Describe the morphology of the red blood cells.
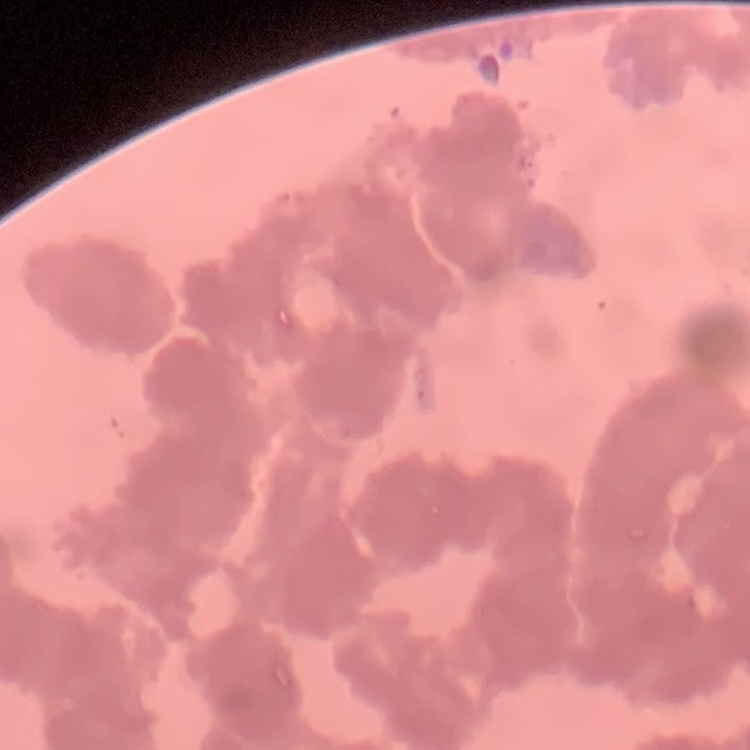
They show rouleaux formation.

Thin peripheral smear. Field's or Giemsa stain. One tile cut from a larger photomicrograph.